Find each white blood cell.
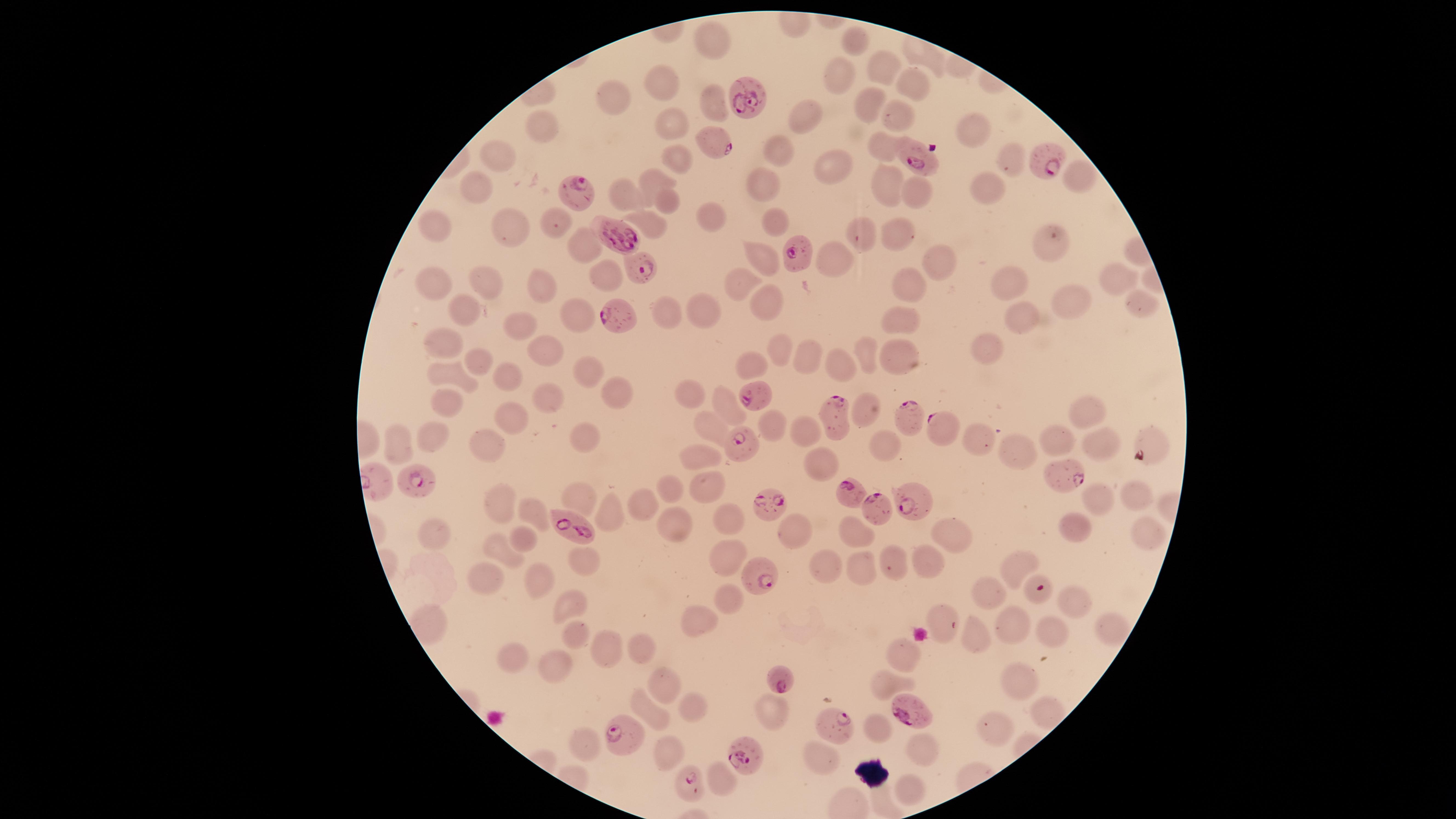

No white blood cells identified.

field of view = single
visible region = circular
capture = smartphone photograph through the microscope eyepiece
presence = malaria parasites detected
stain = Giemsa
species = Plasmodium falciparum
preparation = thin blood film
parasitized red blood cells = approximate marker points, in pixels from the top-left corner: (x=749, y=98), (x=710, y=138), (x=1042, y=161), (x=914, y=162), (x=582, y=193), (x=608, y=230), (x=792, y=253), (x=641, y=264), (x=618, y=314), (x=759, y=395), (x=838, y=412), (x=912, y=417), (x=944, y=428), (x=738, y=441), (x=1060, y=478), (x=425, y=481), (x=850, y=492), (x=906, y=495), (x=765, y=505), (x=875, y=507), (x=572, y=527), (x=755, y=571), (x=778, y=684), (x=911, y=709), (x=834, y=726), (x=623, y=736), (x=745, y=756), (x=685, y=782)
uninfected red blood cells = approximate marker points, in pixels from the top-left corner: (x=710, y=37), (x=853, y=47), (x=922, y=58), (x=883, y=70), (x=843, y=77), (x=663, y=81), (x=909, y=87), (x=613, y=99), (x=710, y=103), (x=869, y=105), (x=895, y=117), (x=804, y=121), (x=671, y=128), (x=971, y=130), (x=548, y=134), (x=880, y=146), (x=770, y=150), (x=677, y=156), (x=501, y=161), (x=1010, y=161), (x=832, y=168), (x=1076, y=174), (x=656, y=179), (x=764, y=182), (x=888, y=187), (x=475, y=188), (x=985, y=189), (x=627, y=193), (x=920, y=196), (x=665, y=200), (x=710, y=215), (x=554, y=223), (x=776, y=223), (x=436, y=224), (x=653, y=226), (x=511, y=230), (x=892, y=234), (x=858, y=237), (x=578, y=242), (x=1051, y=242), (x=760, y=252), (x=833, y=259), (x=940, y=263), (x=605, y=266), (x=485, y=281), (x=1003, y=281), (x=1116, y=281), (x=433, y=283), (x=903, y=285), (x=540, y=287), (x=742, y=287), (x=1068, y=302), (x=1138, y=303), (x=465, y=306), (x=767, y=306), (x=696, y=307), (x=670, y=314), (x=580, y=316), (x=1023, y=319), (x=519, y=324), (x=901, y=324), (x=439, y=337), (x=990, y=344), (x=542, y=350), (x=780, y=350), (x=863, y=355), (x=478, y=359), (x=807, y=359), (x=901, y=360), (x=841, y=365), (x=754, y=366), (x=450, y=370), (x=585, y=371), (x=508, y=377), (x=613, y=391), (x=690, y=392), (x=444, y=394), (x=550, y=394), (x=725, y=406), (x=1088, y=409), (x=501, y=410), (x=866, y=414), (x=768, y=427), (x=797, y=428), (x=714, y=430), (x=429, y=434), (x=579, y=437), (x=969, y=438), (x=1053, y=440), (x=1101, y=441), (x=397, y=442), (x=884, y=442), (x=483, y=445), (x=1024, y=454), (x=696, y=457), (x=818, y=462), (x=705, y=484), (x=672, y=489), (x=1132, y=491), (x=582, y=493), (x=639, y=500), (x=510, y=501), (x=1097, y=501), (x=531, y=513), (x=612, y=517), (x=731, y=519), (x=670, y=524), (x=1080, y=526), (x=854, y=529), (x=793, y=530), (x=1147, y=530), (x=430, y=531), (x=947, y=536), (x=522, y=537), (x=502, y=550), (x=726, y=555), (x=930, y=557), (x=893, y=558), (x=578, y=559), (x=863, y=561), (x=1018, y=564), (x=822, y=567), (x=485, y=576), (x=531, y=579), (x=990, y=593), (x=726, y=596), (x=1071, y=600), (x=568, y=604), (x=941, y=616), (x=703, y=620), (x=1014, y=620), (x=1051, y=628), (x=1111, y=630), (x=571, y=633), (x=978, y=638), (x=605, y=645), (x=639, y=647), (x=510, y=654), (x=896, y=654), (x=556, y=665), (x=1014, y=673), (x=884, y=679), (x=660, y=684), (x=691, y=709), (x=775, y=711), (x=649, y=712), (x=1051, y=712), (x=872, y=724), (x=990, y=726), (x=591, y=742), (x=662, y=749), (x=926, y=749), (x=823, y=754), (x=718, y=780), (x=901, y=789), (x=881, y=802)
image size = 1456×819 pixels